Assess this cell for malaria.
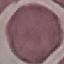

It is uninfected.

preparation: thin blood smear
capture: smartphone through the microscope eyepiece
stain: Giemsa
image_type: cell patch, automatically extracted from a larger field of view and resized to 64 × 64 pixels